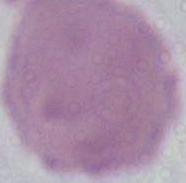

Summary:
  - Magnification: 1000x
  - Identification: erythrocyte
  - Modality: photomicrograph